Outline each blood parasite and name the species.
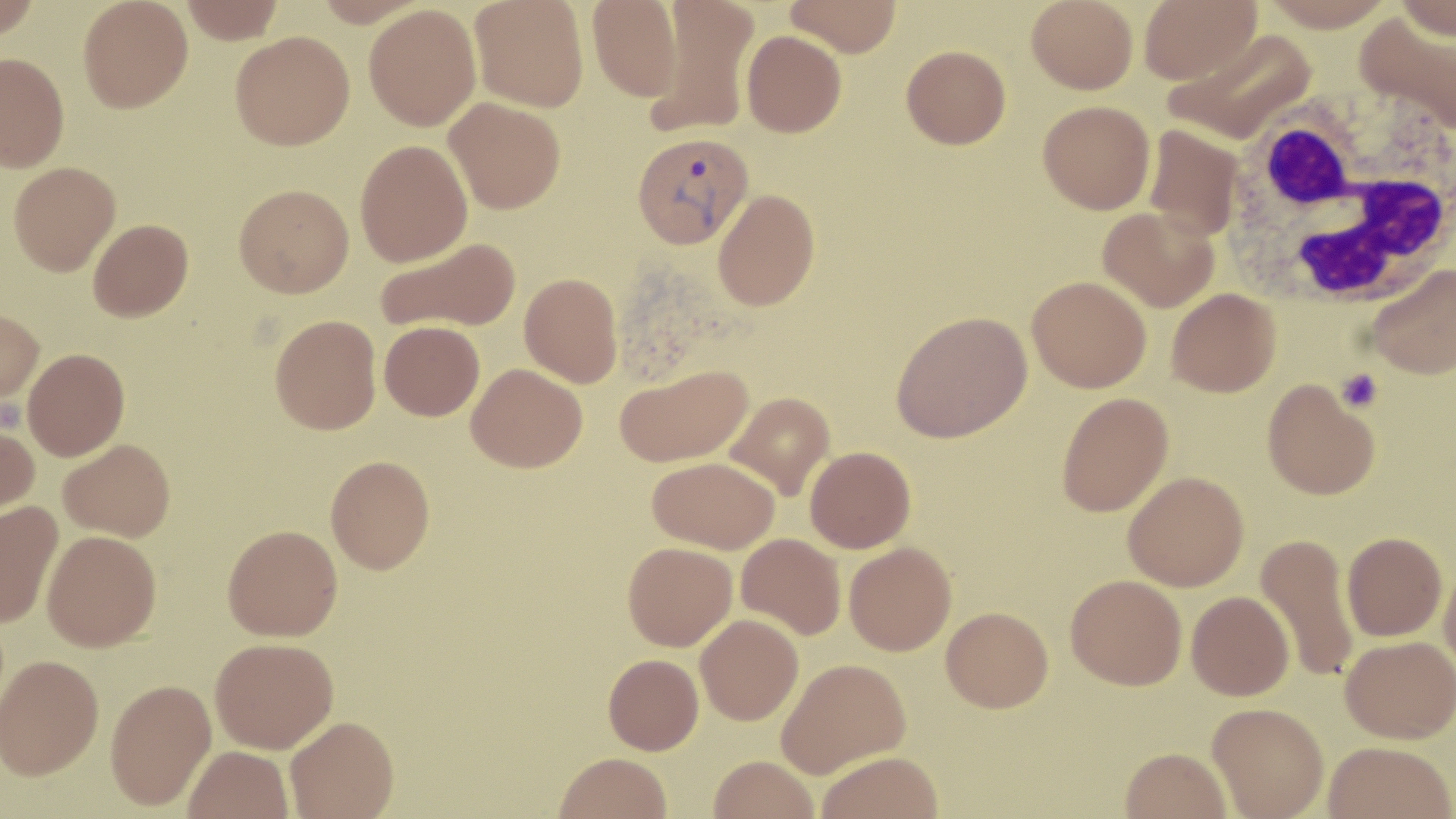

Approximate bounding boxes as (x1, y1, x2, y2) in pixels.
Plasmodium vivax-infected red blood cells: (632, 131, 754, 248).
No Plasmodium falciparum, Plasmodium ovale, Plasmodium malariae, Babesia divergens, or Trypanosoma brucei observed.

slide-level diagnosis = Plasmodium vivax
magnification = 1000x
preparation = thin blood film
uninfected red blood cell locations = approximate bounding boxes as (x1, y1, x2, y2) in pixels: (0, 0, 41, 40), (78, 0, 193, 113), (180, 0, 285, 43), (470, 0, 589, 112), (648, 0, 759, 136), (785, 0, 901, 57), (1026, 0, 1138, 94), (1139, 0, 1261, 85), (1393, 0, 1456, 41), (588, 1, 682, 101), (363, 4, 482, 131), (1354, 11, 1456, 138), (1163, 28, 1319, 146), (741, 30, 846, 138), (230, 31, 354, 150), (901, 45, 1011, 149), (0, 53, 69, 172), (444, 96, 566, 214), (1038, 101, 1155, 214), (1143, 125, 1244, 241), (355, 139, 472, 266), (8, 161, 120, 275), (234, 183, 354, 297), (713, 189, 820, 311), (1098, 206, 1220, 312), (88, 218, 194, 321), (375, 236, 521, 333), (1365, 264, 1456, 379), (519, 272, 623, 387), (1027, 275, 1151, 392), (1167, 288, 1280, 397), (0, 308, 44, 405), (890, 310, 1032, 443), (270, 314, 381, 434), (379, 321, 484, 420), (22, 348, 129, 460), (467, 363, 587, 472), (615, 364, 752, 467), (1262, 379, 1379, 499), (723, 391, 836, 501), (1057, 392, 1173, 517), (0, 420, 39, 521), (59, 438, 175, 541), (805, 446, 916, 553), (326, 455, 435, 574), (647, 456, 780, 554), (1123, 471, 1249, 590), (0, 500, 63, 628), (223, 524, 342, 641), (42, 530, 161, 651), (1342, 532, 1447, 641), (737, 533, 846, 639), (1255, 533, 1361, 683), (622, 541, 737, 650), (845, 542, 956, 655), (1438, 558, 1456, 677), (1065, 574, 1187, 690), (1187, 590, 1294, 700), (941, 606, 1053, 712), (695, 614, 803, 725), (1340, 635, 1456, 743), (211, 637, 338, 752), (603, 653, 703, 755), (1, 654, 103, 779), (776, 658, 910, 779), (105, 678, 216, 809), (1207, 702, 1329, 818), (285, 715, 399, 818), (1323, 740, 1454, 819), (183, 745, 294, 819), (1120, 747, 1232, 819), (816, 751, 943, 819), (554, 752, 671, 819), (709, 755, 820, 819)
image size = 1456×819 pixels
white blood cell locations = approximate bounding boxes as (x1, y1, x2, y2) in pixels: (1227, 93, 1456, 312)
stain = May-Grünwald-Giemsa
field of view = one of a larger specimen
modality = light microscopy
platelet locations = approximate bounding boxes as (x1, y1, x2, y2) in pixels: (1337, 369, 1383, 413)